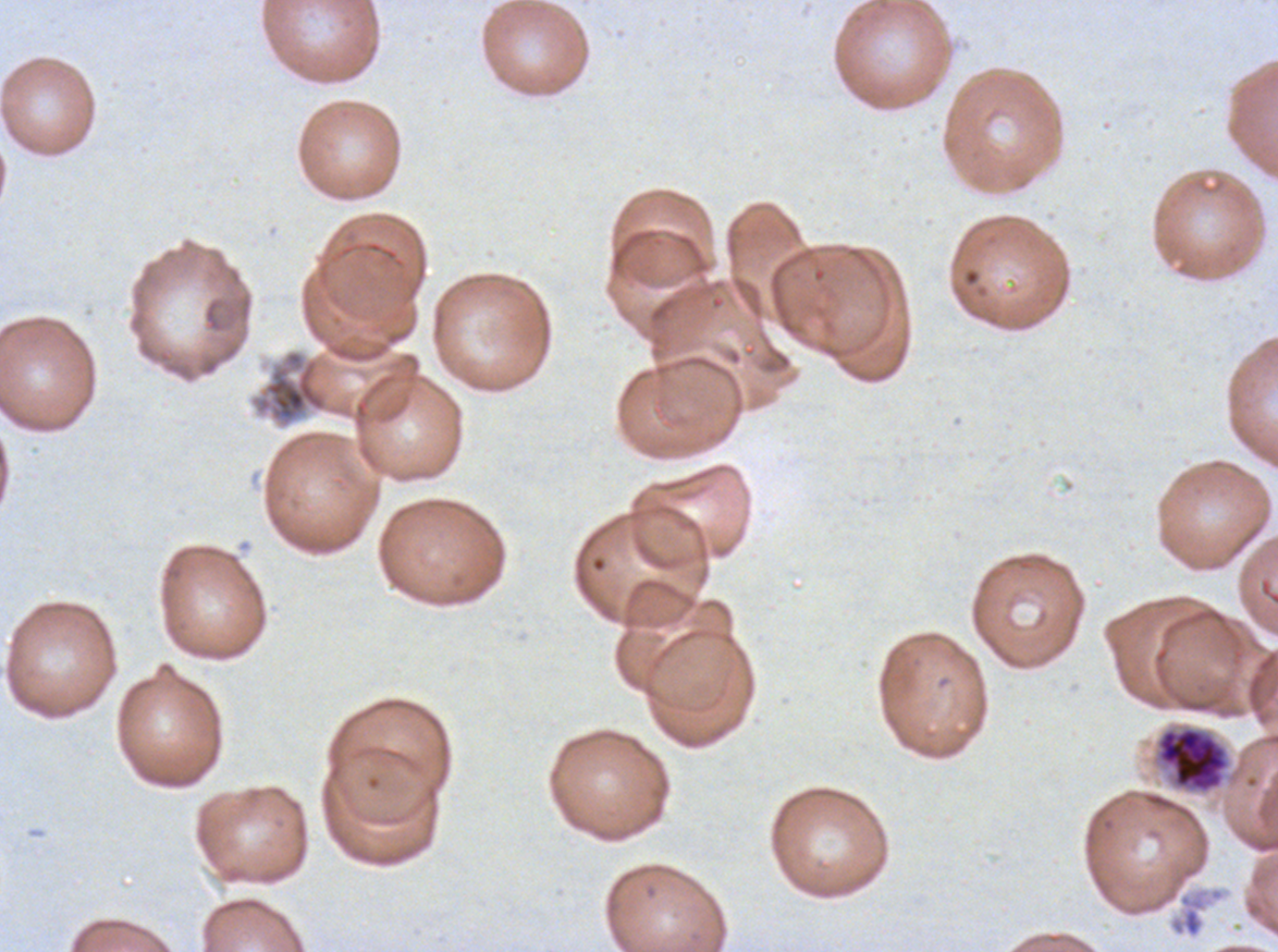 Approximate bounding boxes as {x1, y1, x2, y2} in pixels. Debris locations: {1172, 899, 1202, 937}. Early schizont locations: {1154, 725, 1232, 796}. Segmenter locations: {255, 349, 328, 426}. Thin blood film. Ex-vivo P. falciparum culture from a patient in The Gambia, grown for 24 to 48 hours. Life-cycle stages observed: early schizont, segmenter. Image is 1278×952 pixels. One sub-image of a larger composite. Giemsa stain.